Identify the parasite.
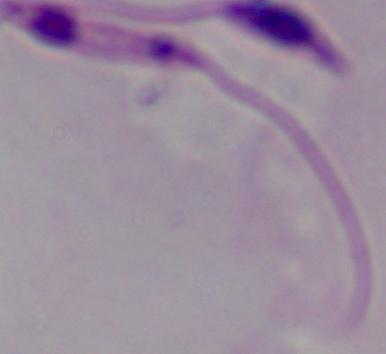

This is Leishmania.

Summary:
  - Modality: photomicrograph
  - Magnification: 1000x